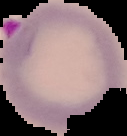
From a thin blood film. Segmented cell region on a black background. Malaria status: parasitized. Image is 127×136 pixels.